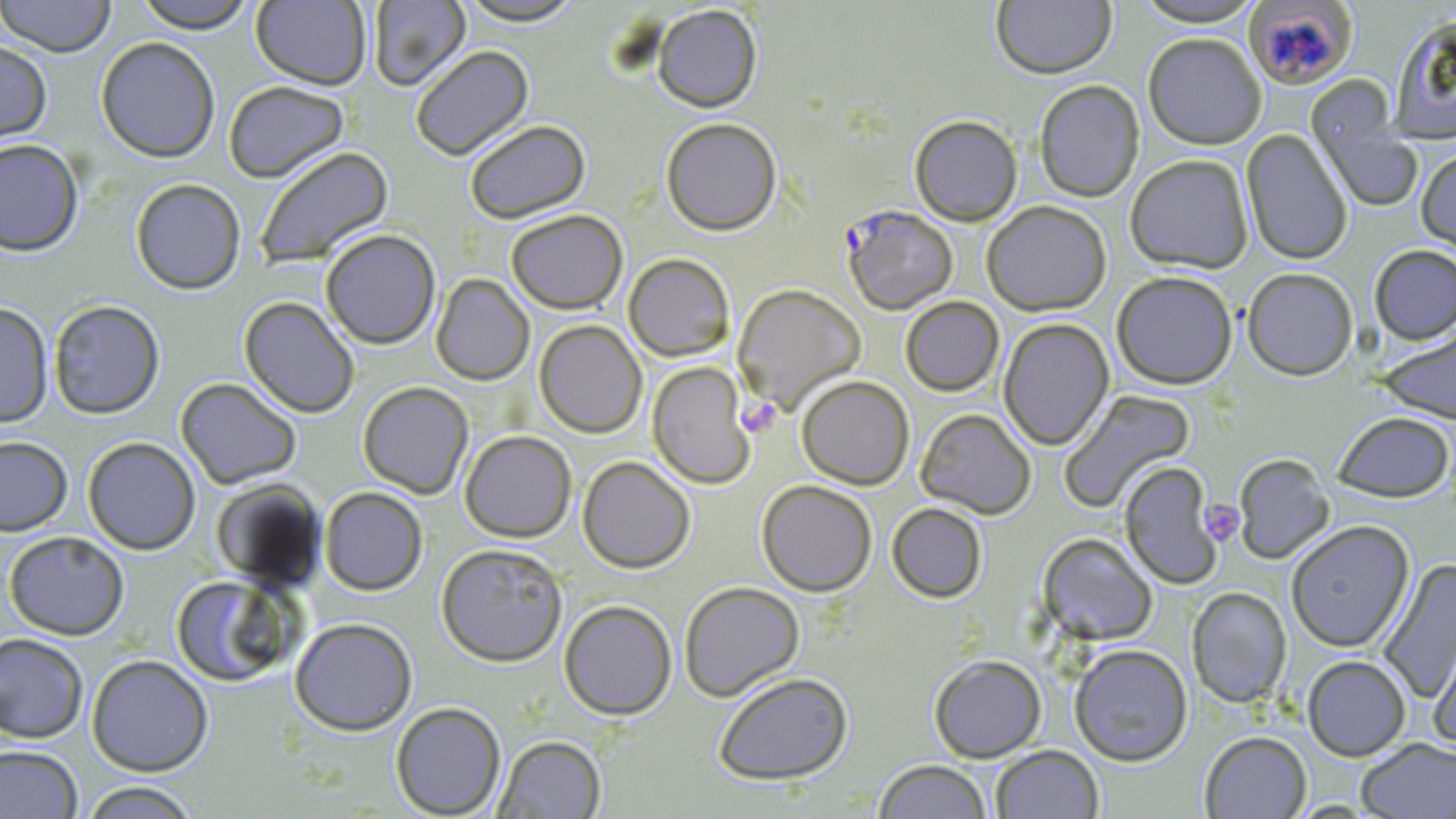
slide_level_diagnosis: Plasmodium falciparum
stain: May-Grünwald-Giemsa
uninfected_red_blood_cell_locations: 'approximate bounding boxes as [x1, y1, x2, y2] in pixels: [0, 0, 117, 57], [132, 0, 257, 33], [251, 0, 371, 90], [367, 0, 471, 91], [1129, 0, 1268, 27], [1247, 0, 1363, 94], [453, 1, 588, 26], [991, 1, 1116, 78], [652, 5, 763, 113], [1389, 13, 1456, 142], [1143, 32, 1267, 149], [95, 36, 221, 162], [0, 40, 53, 147], [409, 45, 534, 161], [1033, 79, 1145, 202], [222, 81, 351, 183], [1313, 110, 1424, 213], [909, 115, 1022, 226], [661, 118, 782, 235], [464, 120, 590, 223], [1241, 128, 1353, 265], [0, 138, 83, 256], [252, 145, 394, 270], [1416, 147, 1456, 259], [1125, 153, 1254, 273], [131, 178, 246, 295], [981, 200, 1111, 316], [505, 209, 628, 314], [320, 229, 441, 349], [1369, 244, 1456, 345], [623, 253, 735, 362], [1242, 267, 1358, 381], [1111, 270, 1238, 390], [431, 273, 534, 386], [733, 282, 867, 414], [239, 296, 360, 418], [900, 296, 1004, 396], [48, 299, 165, 419], [0, 302, 54, 428], [998, 318, 1114, 450], [534, 320, 647, 438], [1373, 326, 1456, 424], [646, 362, 756, 489], [796, 375, 914, 489], [175, 377, 302, 489], [357, 381, 473, 499], [1057, 388, 1196, 513], [915, 408, 1036, 520], [1332, 411, 1455, 503], [460, 430, 576, 542], [0, 436, 73, 536], [83, 437, 200, 555], [1233, 454, 1334, 564], [578, 456, 696, 574], [1119, 461, 1223, 589], [210, 478, 326, 592], [757, 480, 877, 597], [319, 487, 428, 595], [887, 503, 987, 604], [1285, 520, 1414, 653], [4, 531, 130, 640], [1037, 532, 1158, 645], [436, 543, 568, 667], [1378, 559, 1456, 703], [170, 575, 295, 687], [679, 581, 805, 702], [1188, 586, 1292, 708], [559, 599, 677, 720], [290, 617, 418, 735], [1429, 628, 1456, 755], [0, 632, 89, 743], [1069, 643, 1193, 766], [86, 654, 213, 776], [929, 654, 1046, 761], [1302, 655, 1411, 761], [713, 672, 853, 785], [391, 702, 506, 818], [1200, 731, 1311, 818], [494, 735, 606, 818], [1356, 737, 1456, 819], [0, 745, 83, 818], [990, 745, 1103, 818], [873, 760, 993, 818], [76, 781, 203, 818]'
field_of_view: one of a larger specimen
modality: light microscopy
preparation: thin blood smear
plasmodium_falciparum_infected_red_blood_cell_locations: 'approximate bounding boxes as [x1, y1, x2, y2] in pixels: [842, 205, 959, 314]'
magnification: 1000x
image_size: 1456×819 pixels
platelet_locations: 'approximate bounding boxes as [x1, y1, x2, y2] in pixels: [738, 397, 781, 437], [1200, 500, 1244, 545]'